Point out each Plasmodium parasite.
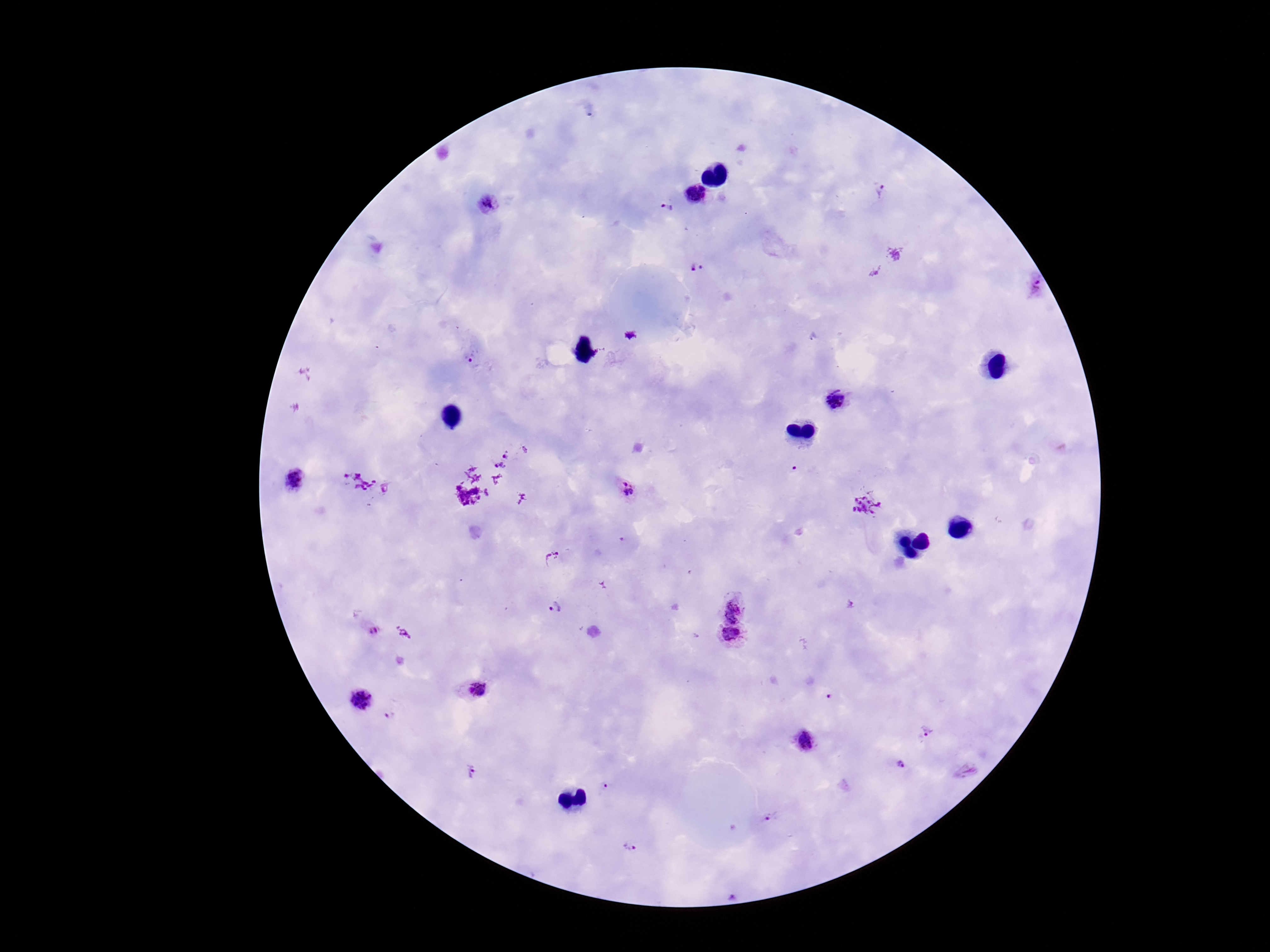
Approximate centers as {x, y} in pixels.
Plasmodium parasites: {882, 191}, {695, 194}, {490, 204}, {667, 208}, {696, 268}, {1036, 286}, {473, 359}, {835, 400}, {508, 453}, {498, 467}, {794, 469}, {293, 480}, {363, 483}, {627, 491}, {864, 506}, {554, 558}, {735, 606}, {557, 609}, {373, 631}, {730, 637}, {473, 689}, {830, 698}, {361, 700}, {388, 718}, {926, 730}, {808, 743}, {901, 764}, {472, 771}, {606, 788}, {770, 819}, {630, 846}.

patient malaria status = infected
magnification = 100x
preparation = thick blood film
image size = 1270×952 pixels
field of view = single
capture = smartphone camera through the microscope eyepiece
stain = Giemsa